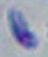

Summary:
  - Modality: micrograph
  - Magnification: 1000x
  - Identification: Toxoplasma gondii